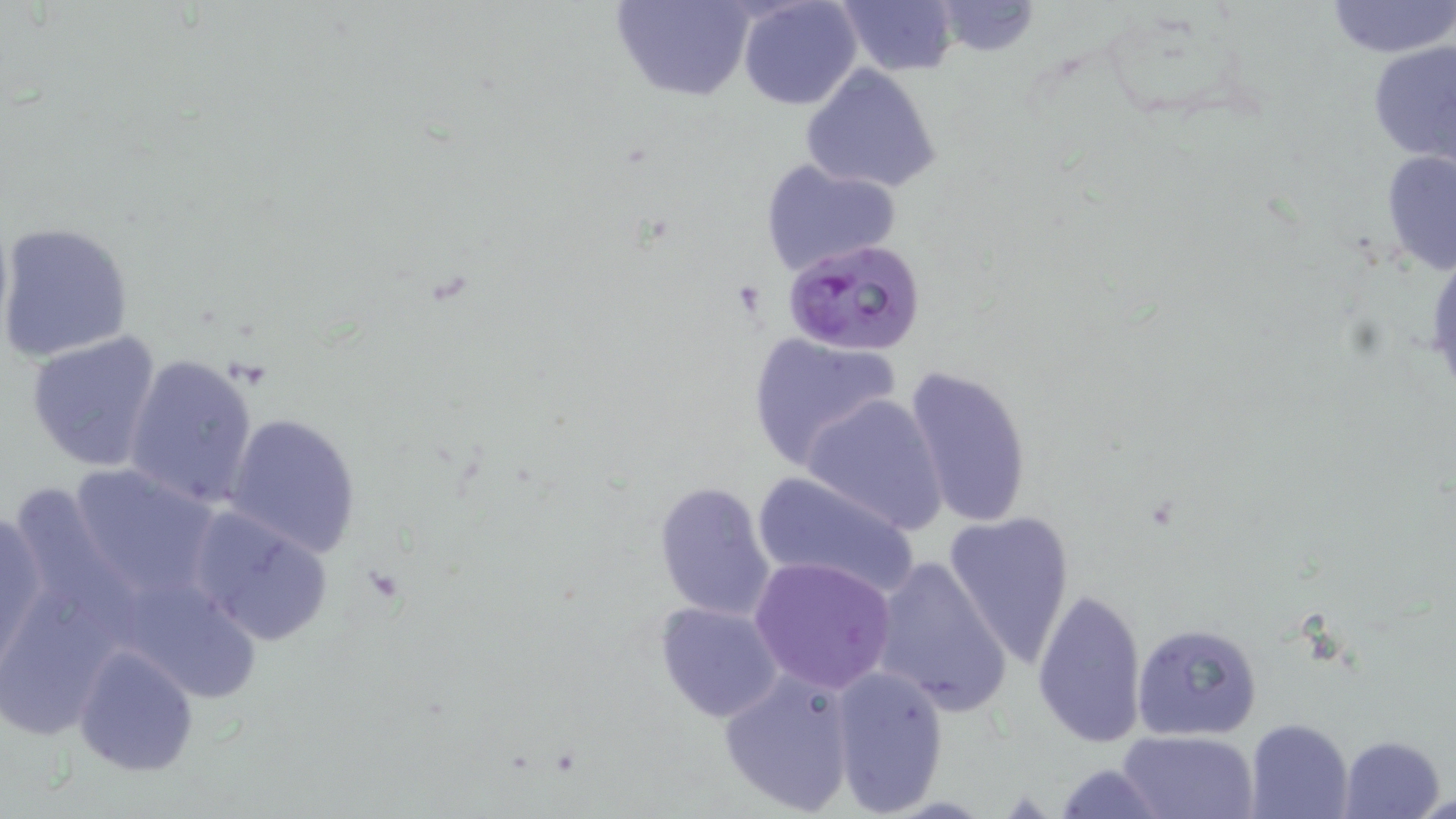
Approximate bounding boxes as [x1, y1, x2, y2] in pixels. Uninfected red blood cell locations: [610, 0, 755, 102], [737, 0, 862, 111], [1325, 0, 1456, 58], [835, 1, 959, 77], [934, 1, 1039, 57], [755, 17, 896, 152], [1367, 41, 1456, 166], [800, 63, 944, 195], [1381, 148, 1456, 277], [758, 158, 902, 277], [1, 221, 135, 362], [24, 330, 166, 472], [746, 330, 904, 472], [122, 353, 258, 509], [902, 362, 1035, 530], [802, 392, 949, 534], [222, 412, 364, 558], [65, 462, 225, 607], [751, 473, 924, 600], [653, 481, 778, 622], [186, 504, 336, 648], [1, 507, 48, 673], [942, 510, 1076, 669], [749, 555, 898, 693], [869, 556, 1012, 714], [1, 580, 125, 735], [1032, 592, 1147, 745], [654, 600, 785, 722], [1131, 621, 1263, 742], [72, 643, 198, 777], [829, 665, 950, 814], [718, 667, 858, 814], [1245, 718, 1353, 819], [1119, 730, 1257, 818], [1340, 735, 1446, 819], [1052, 761, 1165, 819], [1420, 790, 1455, 818]. Plasmodium falciparum-infected red blood cell locations: [781, 237, 927, 357]. Slide-level diagnosis: Plasmodium falciparum. Optical microscopy. Captured at 1000x magnification. One field of a larger specimen. May-Grünwald-Giemsa-stained preparation. Thin blood film. Image is 1456×819 pixels.